Locate platelets.
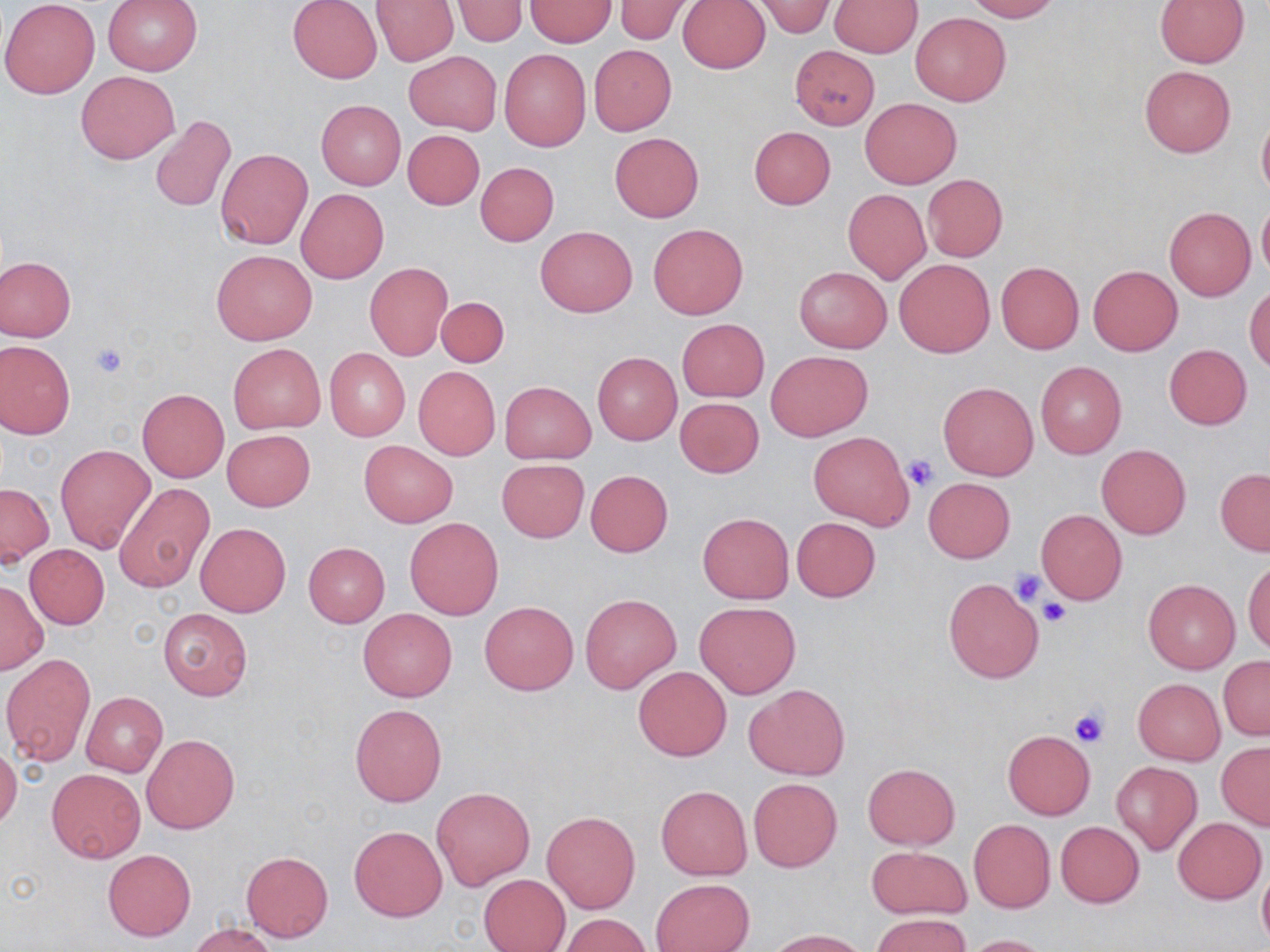
Approximate bounding boxes as (x1, y1, x2, y2) in pixels.
Platelets: (89, 342, 128, 379), (903, 453, 939, 492), (1011, 568, 1048, 605), (1027, 582, 1070, 618), (1037, 599, 1070, 628), (1069, 704, 1110, 746).

Summary:
  - Uninfected red blood cell locations: (0, 0, 99, 99), (102, 0, 202, 76), (287, 0, 383, 83), (370, 0, 457, 65), (452, 0, 528, 47), (612, 0, 695, 44), (678, 0, 770, 73), (831, 0, 922, 56), (964, 0, 1058, 21), (524, 1, 616, 47), (756, 1, 837, 39), (1154, 1, 1250, 67), (910, 12, 1010, 105), (588, 44, 677, 136), (789, 45, 879, 130), (498, 48, 591, 151), (404, 51, 500, 134), (1139, 65, 1235, 157), (76, 70, 180, 164), (860, 98, 961, 189), (316, 100, 406, 190), (1257, 112, 1270, 202), (151, 114, 236, 212), (748, 126, 836, 209), (403, 131, 485, 209), (609, 132, 703, 222), (215, 147, 312, 250), (475, 162, 559, 246), (922, 174, 1007, 261), (296, 189, 390, 284), (843, 189, 931, 283), (1257, 200, 1270, 280), (1165, 207, 1256, 300), (648, 224, 748, 320), (537, 225, 637, 317), (211, 248, 317, 345), (0, 256, 76, 341), (894, 258, 995, 357), (996, 261, 1082, 353), (365, 263, 452, 360), (1088, 265, 1182, 355), (795, 266, 892, 353), (1245, 285, 1270, 372), (437, 296, 509, 368), (676, 318, 770, 402), (0, 340, 76, 438), (228, 343, 325, 433), (1164, 344, 1252, 429), (324, 348, 410, 441), (766, 350, 872, 440), (593, 352, 681, 444), (1035, 361, 1126, 458), (413, 366, 500, 459), (499, 380, 596, 464), (938, 382, 1037, 480), (137, 389, 228, 482), (674, 396, 764, 478), (222, 429, 315, 511), (807, 430, 914, 531), (359, 440, 458, 527), (56, 444, 154, 552), (1097, 444, 1191, 539), (497, 459, 589, 542), (1215, 468, 1270, 555), (585, 470, 673, 557), (923, 477, 1015, 563), (1, 483, 53, 565), (114, 484, 213, 590), (1036, 510, 1127, 604), (698, 512, 793, 603), (792, 517, 881, 601), (405, 518, 503, 619), (196, 523, 290, 616), (304, 542, 389, 627), (25, 544, 109, 629), (1244, 560, 1270, 656), (943, 579, 1043, 683), (1143, 579, 1240, 674), (0, 580, 46, 675), (580, 592, 682, 694), (480, 601, 579, 695), (695, 601, 801, 699), (158, 608, 254, 700), (358, 608, 458, 701), (2, 654, 95, 765), (1218, 656, 1270, 740), (634, 665, 731, 761), (1133, 678, 1225, 765), (745, 683, 850, 780), (82, 691, 167, 776), (350, 704, 447, 807), (1003, 730, 1095, 818), (142, 734, 239, 834), (1216, 742, 1270, 829), (0, 747, 21, 830), (1112, 762, 1202, 854), (862, 763, 960, 849), (47, 769, 144, 863), (748, 778, 841, 871), (655, 785, 752, 880), (432, 786, 535, 890), (542, 810, 640, 912), (1173, 817, 1265, 904), (968, 820, 1056, 912), (1054, 821, 1144, 907), (350, 825, 447, 922), (866, 845, 971, 919), (103, 849, 195, 941), (242, 851, 334, 942), (1257, 858, 1270, 949), (478, 874, 570, 952), (651, 878, 754, 952), (872, 913, 971, 952), (561, 914, 651, 951), (188, 923, 278, 952), (769, 929, 868, 952), (962, 934, 1053, 952)
  - Slide-level diagnosis: negative for blood parasites
  - Image size: 1270×952 pixels
  - Preparation: thin blood smear
  - Modality: optical microscopy
  - Stain: May-Grünwald-Giemsa
  - Field of view: one of a larger specimen
  - Magnification: 1000x